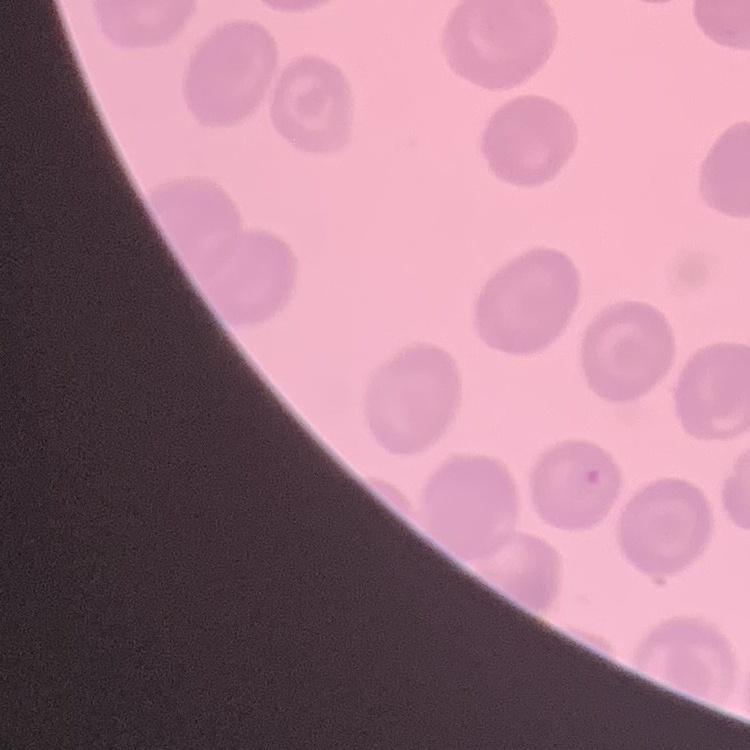

The erythrocytes show no rouleaux formation. One tile cut from a larger photomicrograph. Thin peripheral smear. Field's or Giemsa stain.